Locate every Plasmodium parasite.
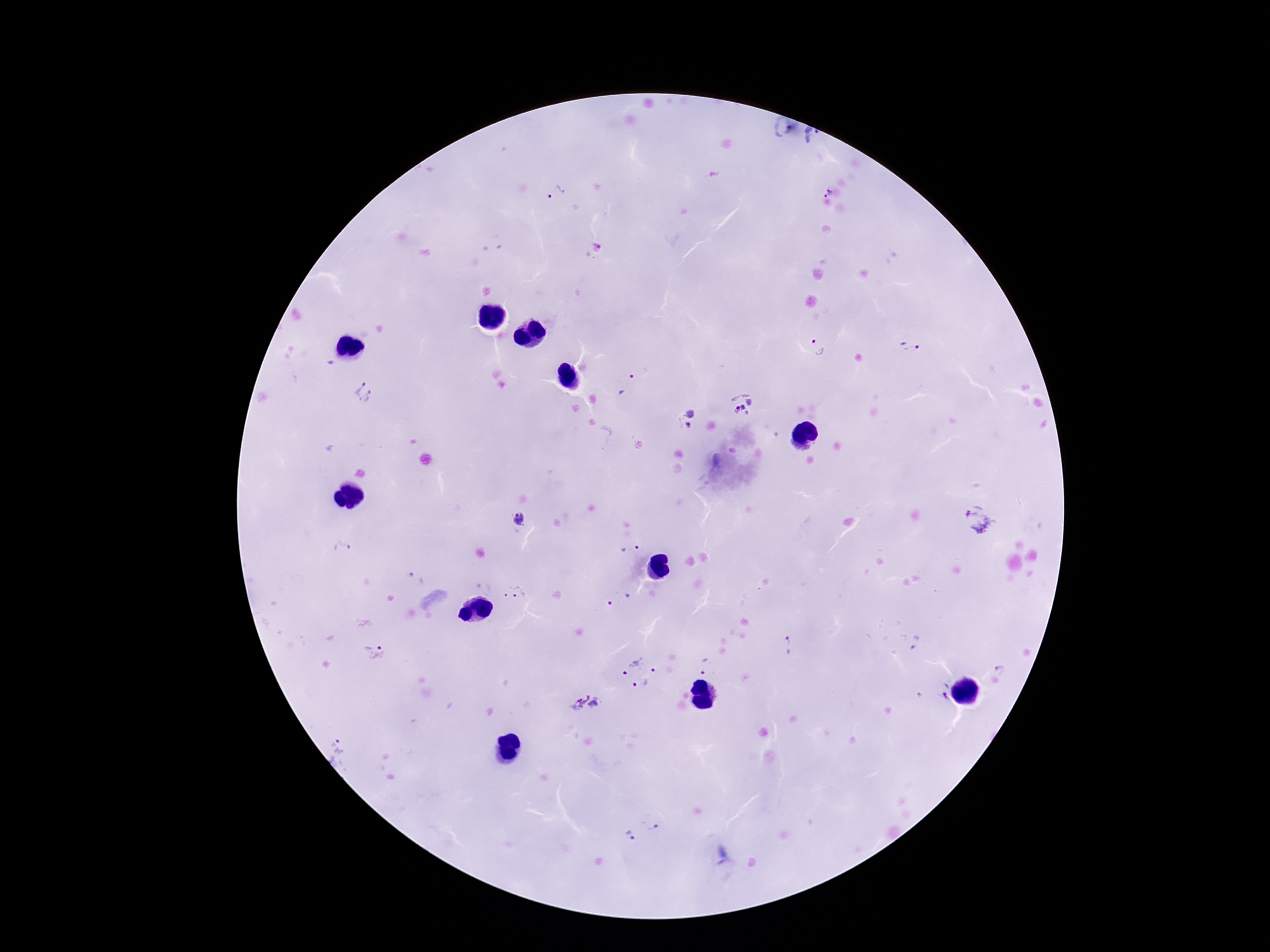
Approximate centers as [x, y] in pixels.
Plasmodium parasites: [811, 136], [555, 192], [827, 193], [819, 346], [910, 347], [627, 386], [365, 390], [743, 403], [686, 420], [519, 519], [978, 520], [340, 549], [629, 549], [415, 578], [516, 593], [619, 599], [375, 642], [787, 645], [920, 646], [707, 666], [1000, 668], [638, 672], [944, 690], [585, 703], [337, 751], [653, 824], [631, 835].

Summary:
  - Preparation: thick peripheral-blood smear
  - Stain: Giemsa
  - Field of view: single
  - Image size: 1270×952 pixels
  - Magnification: 100x
  - Capture: smartphone camera through the microscope eyepiece
  - Patient malaria status: infected